Classify this cell by malaria status.
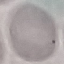

Uninfected.

preparation = thin smear
capture = smartphone camera at the microscope eyepiece
image type = cell patch, automatically extracted from a larger field of view and resized to 64 × 64 pixels
stain = Giemsa